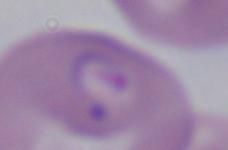

Summary:
  - Modality: photomicrograph
  - Identification: Babesia
  - Magnification: 1000x